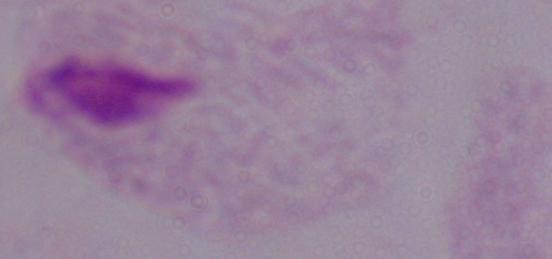

Micrograph. Captured at 1000x magnification. A trichomonad is seen.